Identify the parasite.
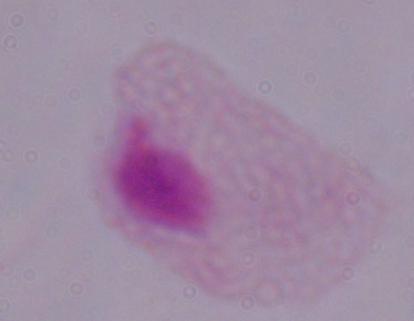

This is a trichomonad.

modality = micrograph
magnification = 1000x